Describe the morphology of the red blood cells.
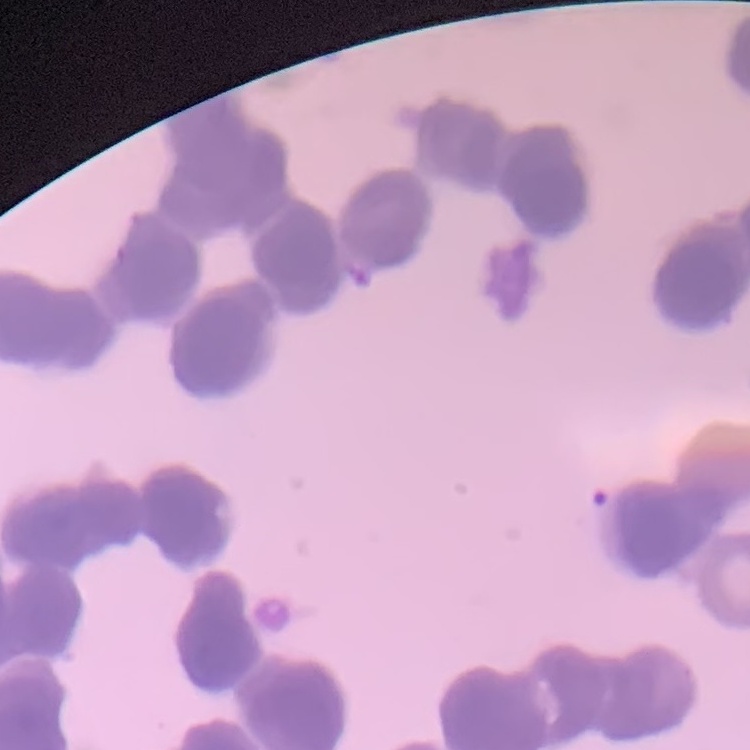

They show rouleaux formation.

stain = Field's or Giemsa
image type = one tile cut from a larger photomicrograph
preparation = thin peripheral smear